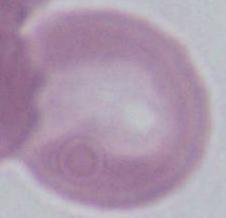
Micrograph. 1000x magnification. A red blood cell is seen.